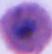 Micrograph. A Plasmodium parasite is seen. Captured at either 400x or 1000x magnification.